Give the position of every Plasmodium parasite visible.
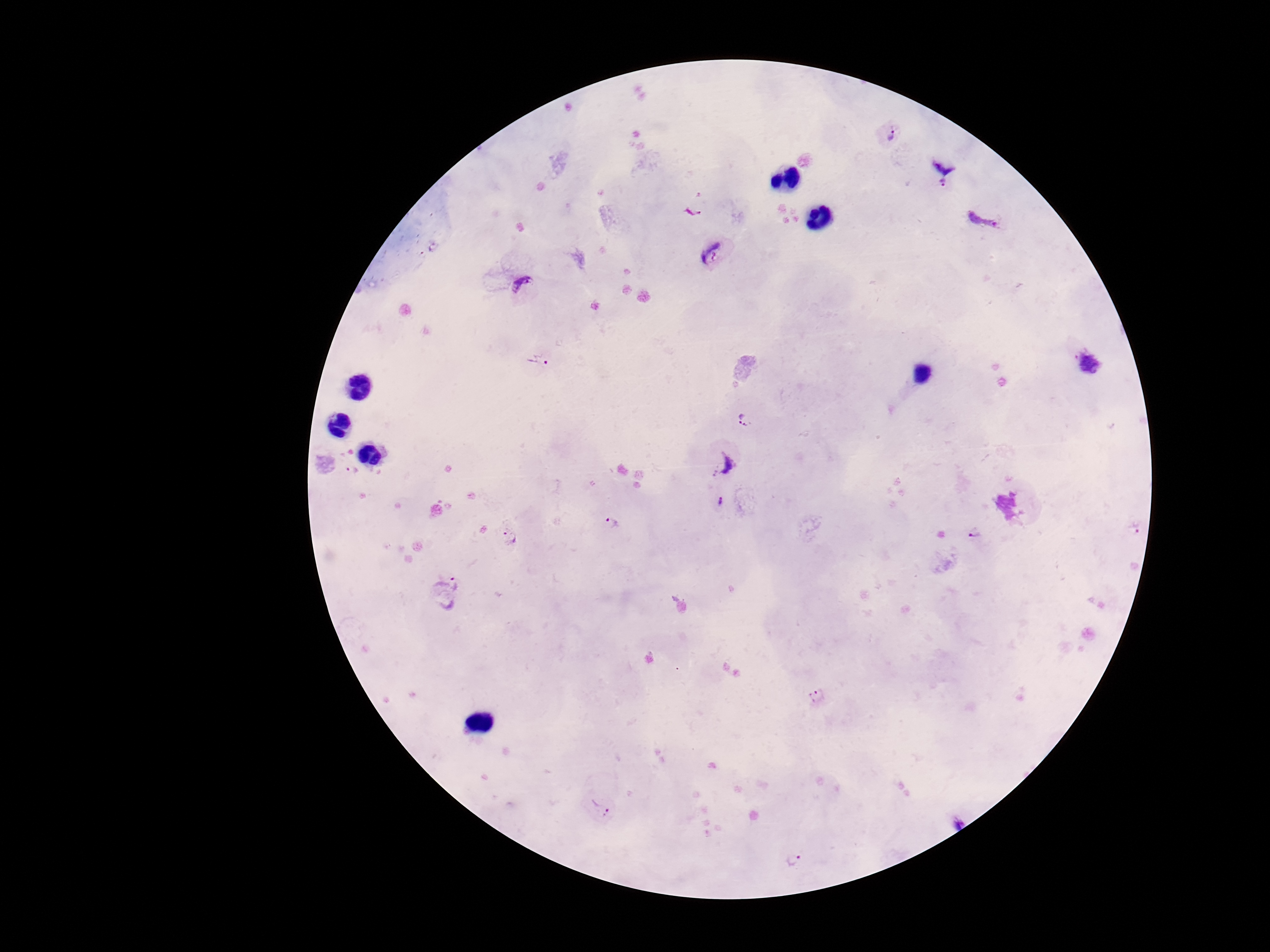
Approximate object centers, in pixels from the top-left corner.
Plasmodium parasites: (x=890, y=134), (x=947, y=161), (x=942, y=188), (x=982, y=221), (x=434, y=247), (x=711, y=253), (x=422, y=256), (x=524, y=289), (x=538, y=360), (x=1090, y=363), (x=744, y=419), (x=724, y=463), (x=351, y=471), (x=721, y=502), (x=613, y=522), (x=1137, y=525), (x=975, y=532), (x=507, y=538), (x=449, y=592), (x=819, y=698), (x=600, y=808), (x=954, y=819), (x=792, y=861).

Summary:
  - Magnification: 100x
  - Field of view: one from this slide
  - Stain: Giemsa
  - Capture: smartphone camera through the microscope eyepiece
  - Preparation: thick blood film
  - Image size: 1270×952 pixels
  - Patient malaria status: positive